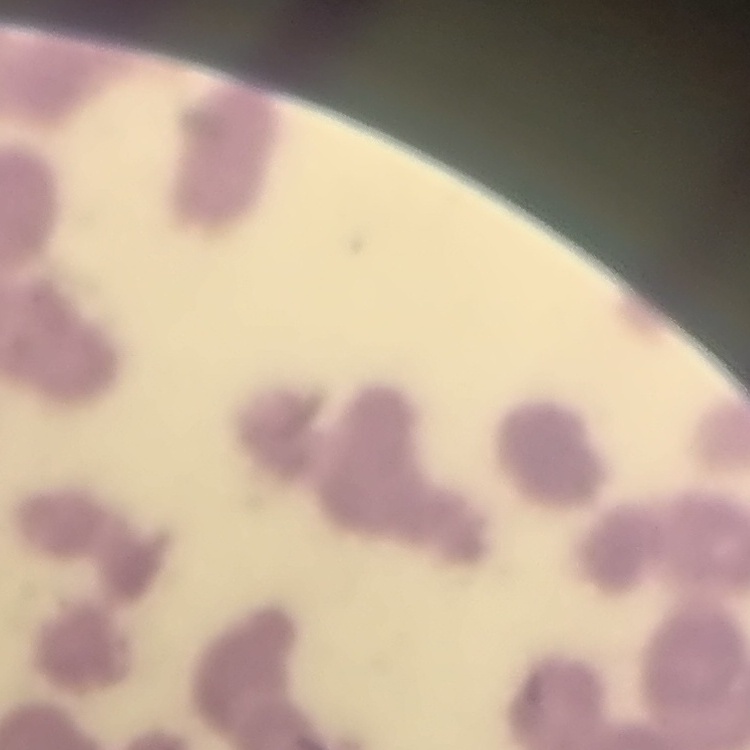 The erythrocytes show rouleaux formation. Square crop of a larger photomicrograph. Thin peripheral smear. Stained with either Field's or Giemsa.